Identify the blood parasite species.
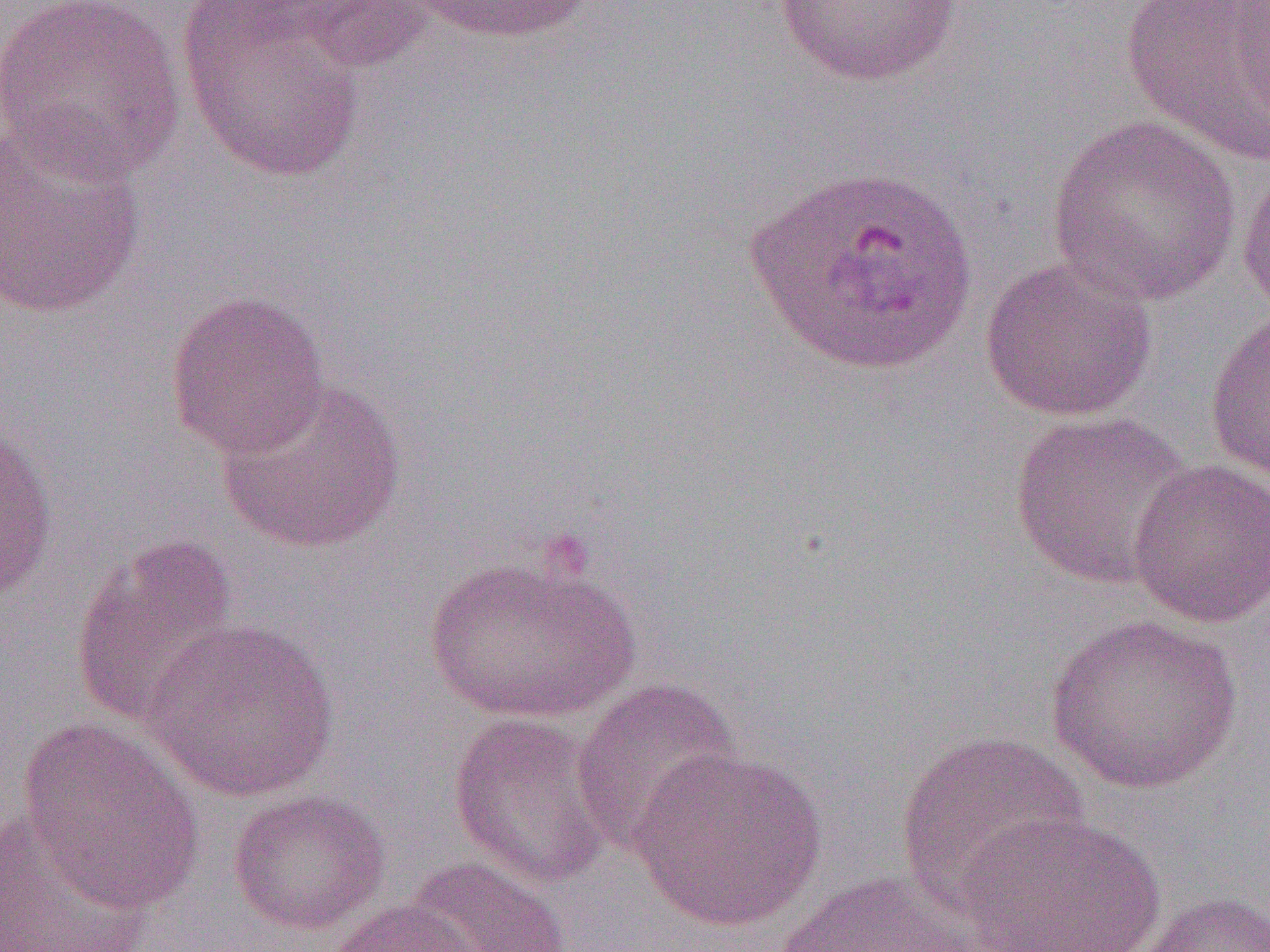

Plasmodium ovale.

{
  "magnification": "1000x",
  "plasmodium_ovale_infected_red_blood_cell_locations": "approximate bounding boxes as named x1/y1/x2/y2 corners in pixels: (x1=744, y1=163, x2=979, y2=375)",
  "field_of_view": "single",
  "modality": "optical microscopy",
  "uninfected_red_blood_cell_locations": "approximate bounding boxes as named x1/y1/x2/y2 corners in pixels: (x1=0, y1=0, x2=186, y2=183), (x1=405, y1=0, x2=601, y2=44), (x1=771, y1=0, x2=965, y2=87), (x1=1119, y1=0, x2=1270, y2=166), (x1=282, y1=2, x2=437, y2=73), (x1=177, y1=3, x2=370, y2=184), (x1=0, y1=114, x2=148, y2=321), (x1=1046, y1=114, x2=1244, y2=307), (x1=1237, y1=163, x2=1270, y2=324), (x1=980, y1=257, x2=1157, y2=423), (x1=163, y1=290, x2=331, y2=460), (x1=1203, y1=306, x2=1270, y2=486), (x1=215, y1=376, x2=407, y2=554), (x1=1007, y1=411, x2=1192, y2=589), (x1=0, y1=423, x2=60, y2=606), (x1=1127, y1=457, x2=1270, y2=628), (x1=69, y1=535, x2=243, y2=730), (x1=422, y1=551, x2=641, y2=724), (x1=1044, y1=613, x2=1243, y2=794), (x1=143, y1=615, x2=339, y2=801), (x1=570, y1=677, x2=743, y2=855), (x1=448, y1=711, x2=618, y2=889), (x1=16, y1=718, x2=206, y2=913), (x1=894, y1=730, x2=1089, y2=914), (x1=630, y1=745, x2=827, y2=931), (x1=227, y1=788, x2=391, y2=935), (x1=0, y1=809, x2=153, y2=952), (x1=956, y1=810, x2=1168, y2=952), (x1=403, y1=855, x2=573, y2=952), (x1=768, y1=870, x2=983, y2=951), (x1=1130, y1=890, x2=1270, y2=952), (x1=323, y1=899, x2=487, y2=952)",
  "preparation": "thin blood smear",
  "image_size": "1270×952 pixels"
}